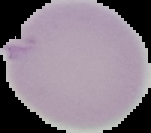
Summary:
  - Image size: 151×133 pixels
  - Result: negative for malaria parasites
  - Preparation: thin blood film
  - Image type: segmented cell region with the area outside set to black